Outline each blood parasite and name the species.
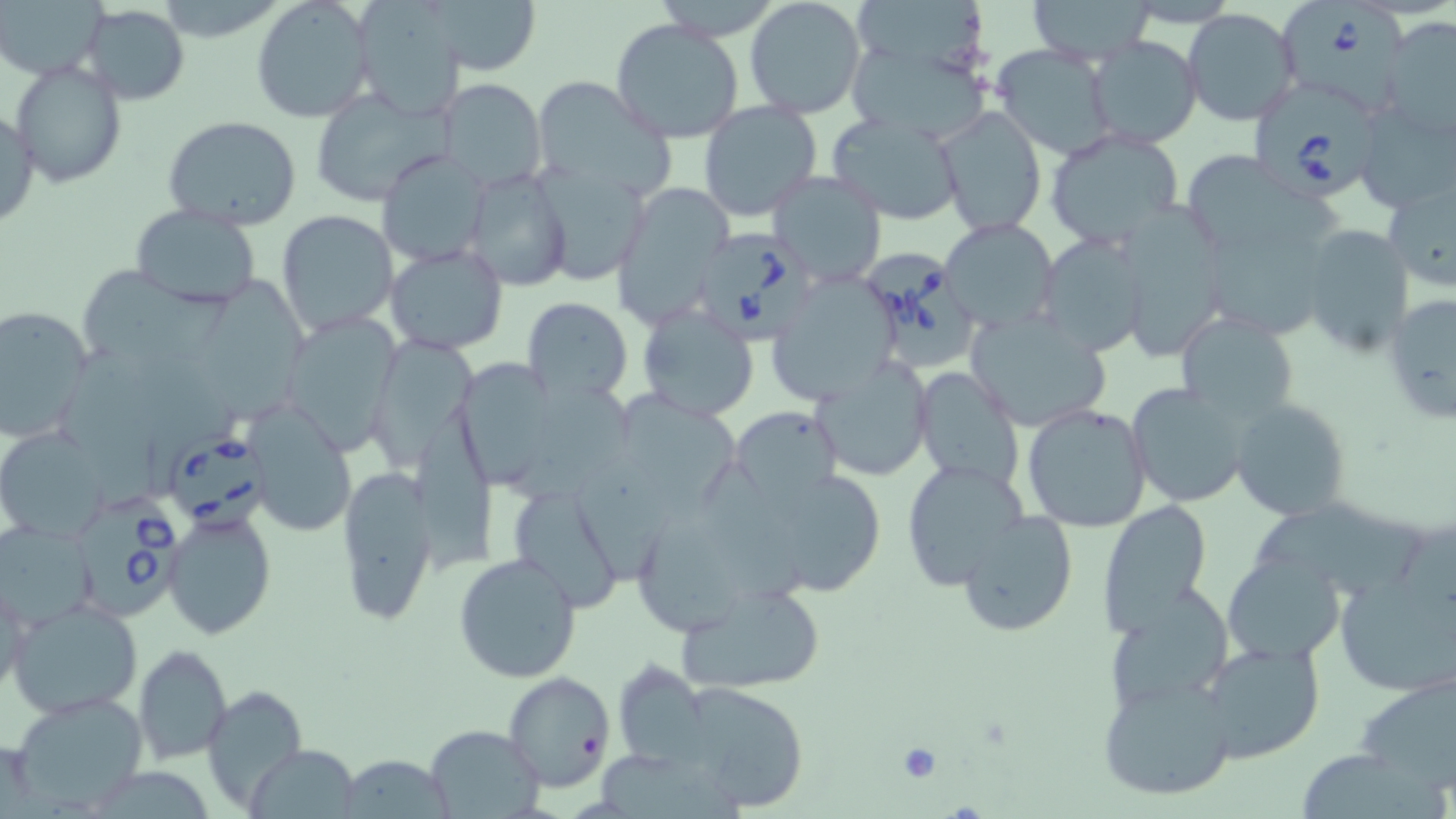

Approximate bounding boxes as named x1/y1/x2/y2 corners in pixels.
Babesia divergens-infected red blood cells: (x1=1284, y1=0, x2=1414, y2=115), (x1=1255, y1=83, x2=1379, y2=207), (x1=691, y1=226, x2=824, y2=345), (x1=868, y1=254, x2=976, y2=372), (x1=169, y1=431, x2=275, y2=534), (x1=73, y1=491, x2=185, y2=621).
No Plasmodium falciparum, Plasmodium ovale, Plasmodium malariae, Plasmodium vivax, or Trypanosoma brucei observed.

slide-level diagnosis = Babesia divergens
stain = May-Grünwald-Giemsa
platelet locations = approximate bounding boxes as named x1/y1/x2/y2 corners in pixels: (x1=897, y1=741, x2=943, y2=783)
field of view = one of a larger specimen
image size = 1456×819 pixels
uninfected red blood cell locations = approximate bounding boxes as named x1/y1/x2/y2 corners in pixels: (x1=0, y1=0, x2=105, y2=81), (x1=430, y1=0, x2=540, y2=76), (x1=744, y1=0, x2=867, y2=119), (x1=1025, y1=0, x2=1158, y2=62), (x1=250, y1=2, x2=373, y2=123), (x1=1122, y1=2, x2=1239, y2=28), (x1=82, y1=3, x2=189, y2=102), (x1=350, y1=3, x2=471, y2=116), (x1=852, y1=4, x2=996, y2=75), (x1=1181, y1=7, x2=1300, y2=126), (x1=611, y1=18, x2=744, y2=143), (x1=1379, y1=18, x2=1456, y2=141), (x1=1085, y1=36, x2=1203, y2=150), (x1=844, y1=39, x2=993, y2=144), (x1=992, y1=45, x2=1116, y2=159), (x1=10, y1=60, x2=126, y2=187), (x1=436, y1=76, x2=548, y2=192), (x1=533, y1=77, x2=676, y2=202), (x1=310, y1=88, x2=452, y2=207), (x1=698, y1=101, x2=821, y2=221), (x1=1354, y1=102, x2=1455, y2=213), (x1=0, y1=105, x2=40, y2=231), (x1=936, y1=107, x2=1045, y2=235), (x1=829, y1=112, x2=965, y2=225), (x1=163, y1=116, x2=303, y2=232), (x1=1045, y1=130, x2=1185, y2=251), (x1=376, y1=148, x2=487, y2=265), (x1=1190, y1=155, x2=1355, y2=277), (x1=532, y1=164, x2=648, y2=286), (x1=464, y1=167, x2=572, y2=293), (x1=768, y1=170, x2=888, y2=288), (x1=1382, y1=178, x2=1456, y2=293), (x1=612, y1=182, x2=734, y2=324), (x1=1113, y1=204, x2=1230, y2=356), (x1=130, y1=205, x2=260, y2=308), (x1=276, y1=209, x2=398, y2=337), (x1=939, y1=217, x2=1058, y2=334), (x1=1299, y1=224, x2=1416, y2=359), (x1=1037, y1=233, x2=1148, y2=356), (x1=385, y1=243, x2=510, y2=353), (x1=81, y1=260, x2=235, y2=369), (x1=207, y1=269, x2=322, y2=424), (x1=767, y1=277, x2=898, y2=406), (x1=1383, y1=293, x2=1455, y2=428), (x1=521, y1=296, x2=634, y2=403), (x1=0, y1=304, x2=94, y2=441), (x1=639, y1=304, x2=760, y2=421), (x1=965, y1=312, x2=1113, y2=432), (x1=1175, y1=312, x2=1302, y2=427), (x1=281, y1=313, x2=402, y2=454), (x1=367, y1=333, x2=480, y2=467), (x1=813, y1=356, x2=933, y2=482), (x1=458, y1=358, x2=569, y2=490), (x1=910, y1=365, x2=1023, y2=492), (x1=1125, y1=382, x2=1253, y2=509), (x1=614, y1=386, x2=749, y2=519), (x1=1228, y1=397, x2=1354, y2=521), (x1=244, y1=402, x2=358, y2=537), (x1=1021, y1=402, x2=1153, y2=533), (x1=731, y1=406, x2=842, y2=511), (x1=0, y1=427, x2=110, y2=542), (x1=902, y1=459, x2=1032, y2=592), (x1=568, y1=460, x2=690, y2=584), (x1=336, y1=463, x2=439, y2=628), (x1=749, y1=463, x2=890, y2=597), (x1=503, y1=480, x2=628, y2=613), (x1=1246, y1=498, x2=1425, y2=608), (x1=1098, y1=499, x2=1213, y2=634), (x1=633, y1=501, x2=745, y2=642), (x1=163, y1=510, x2=277, y2=639), (x1=956, y1=510, x2=1080, y2=639), (x1=1, y1=521, x2=98, y2=630), (x1=1334, y1=551, x2=1454, y2=700), (x1=453, y1=552, x2=582, y2=682), (x1=1222, y1=554, x2=1344, y2=662), (x1=1, y1=574, x2=29, y2=704), (x1=674, y1=580, x2=829, y2=698), (x1=1104, y1=587, x2=1235, y2=714), (x1=8, y1=598, x2=144, y2=718), (x1=1202, y1=638, x2=1326, y2=763), (x1=133, y1=644, x2=232, y2=765), (x1=614, y1=659, x2=710, y2=767), (x1=1353, y1=669, x2=1456, y2=793), (x1=504, y1=672, x2=615, y2=792), (x1=1100, y1=676, x2=1236, y2=804), (x1=677, y1=680, x2=813, y2=813), (x1=201, y1=684, x2=308, y2=811), (x1=9, y1=690, x2=151, y2=814), (x1=424, y1=725, x2=543, y2=817), (x1=247, y1=743, x2=360, y2=819), (x1=1293, y1=746, x2=1443, y2=818), (x1=332, y1=757, x2=459, y2=817)
preparation = thin blood film
magnification = 1000x
modality = light microscopy